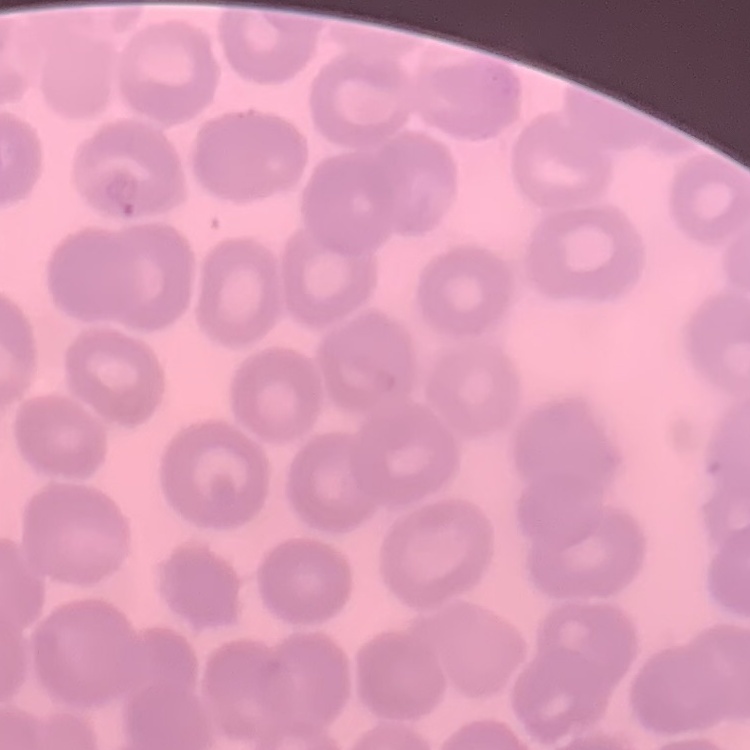
The red blood cells exhibit no rouleaux formation. Square crop of a larger photomicrograph. Thin peripheral smear. Field's or Giemsa stain.